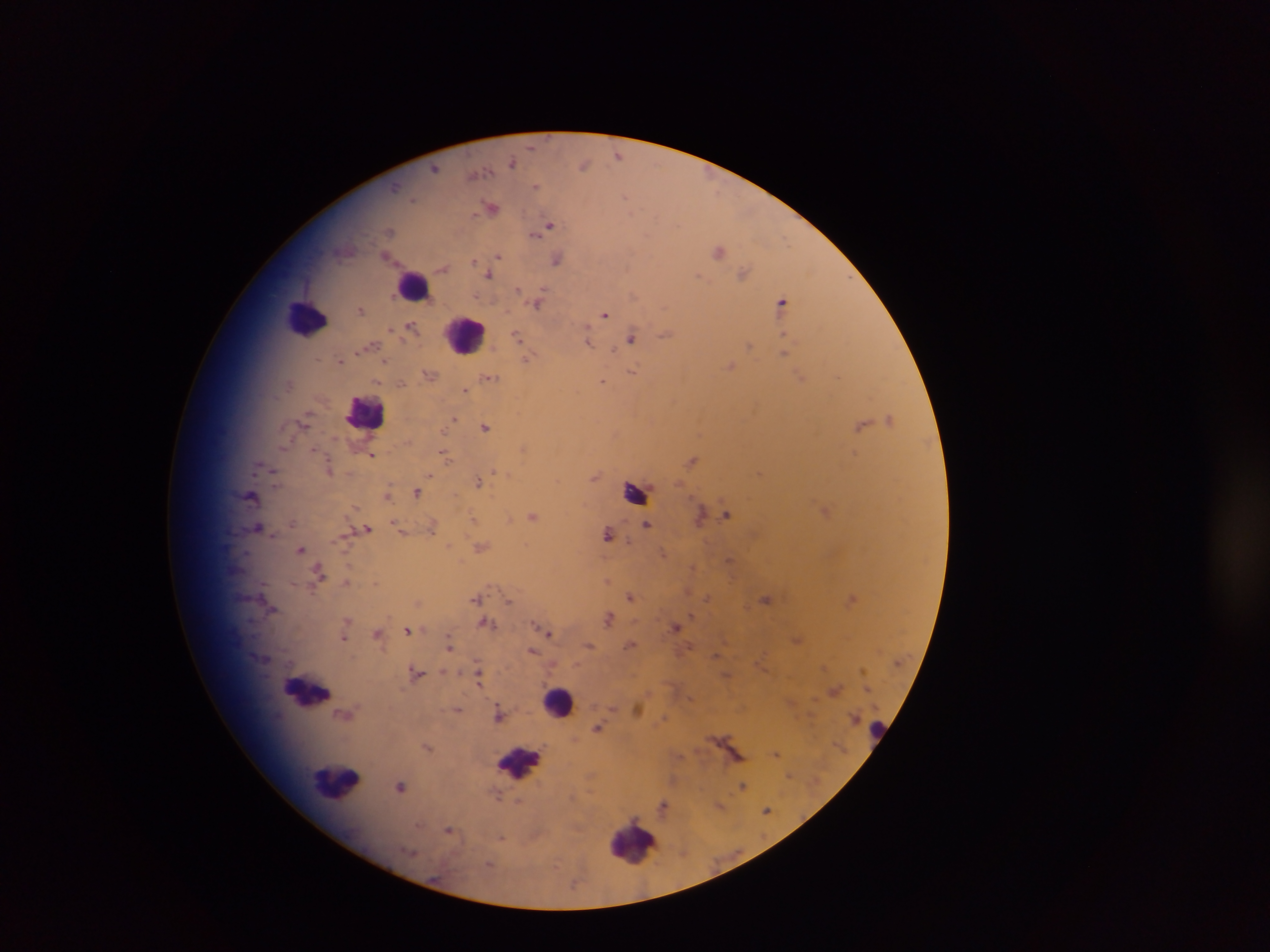
{
  "country": "Ghana",
  "preparation": "thick blood smear",
  "field_of_view": "single",
  "image_size": "1270×952 pixels",
  "leukocyte_locations": "approximate centers as (x, y) in pixels: (416, 286), (305, 316), (465, 333), (362, 411), (555, 699), (338, 780), (634, 842)",
  "malaria_parasite_locations": "approximate centers as (x, y) in pixels: (531, 145), (618, 155), (512, 160), (584, 163), (433, 166), (481, 171), (535, 187), (626, 194), (412, 198), (493, 209), (549, 226), (389, 231), (534, 235), (499, 256), (474, 259), (558, 259), (443, 267), (488, 275), (546, 287), (520, 289), (636, 296), (783, 301), (535, 305), (360, 310), (607, 312), (408, 321), (411, 325), (393, 329), (588, 330), (783, 333), (665, 334), (516, 336), (631, 337), (589, 340), (614, 349), (385, 360), (529, 360), (340, 361), (632, 370), (837, 374), (491, 377), (377, 381), (402, 383), (604, 383), (465, 390), (455, 417), (862, 423), (486, 426), (313, 446), (444, 453), (373, 455), (448, 457), (691, 460), (497, 470), (432, 475), (480, 482), (417, 492), (727, 513), (532, 515), (473, 516), (290, 523), (647, 525), (368, 528), (432, 529), (608, 533), (483, 547), (300, 549), (729, 559), (692, 569), (318, 570), (607, 581), (628, 596), (476, 597), (705, 597), (510, 598), (689, 615), (608, 618), (481, 623), (493, 623), (538, 626), (674, 626), (407, 629), (377, 633), (550, 635), (344, 639), (450, 644), (589, 645), (629, 645), (533, 651), (718, 654), (478, 668), (418, 671), (478, 684), (639, 707), (457, 710), (597, 726), (427, 746), (777, 753), (741, 783), (402, 787), (496, 796), (662, 805), (766, 811), (419, 824), (449, 830), (501, 836)",
  "capture": "mobile-phone photograph through a microscope"
}